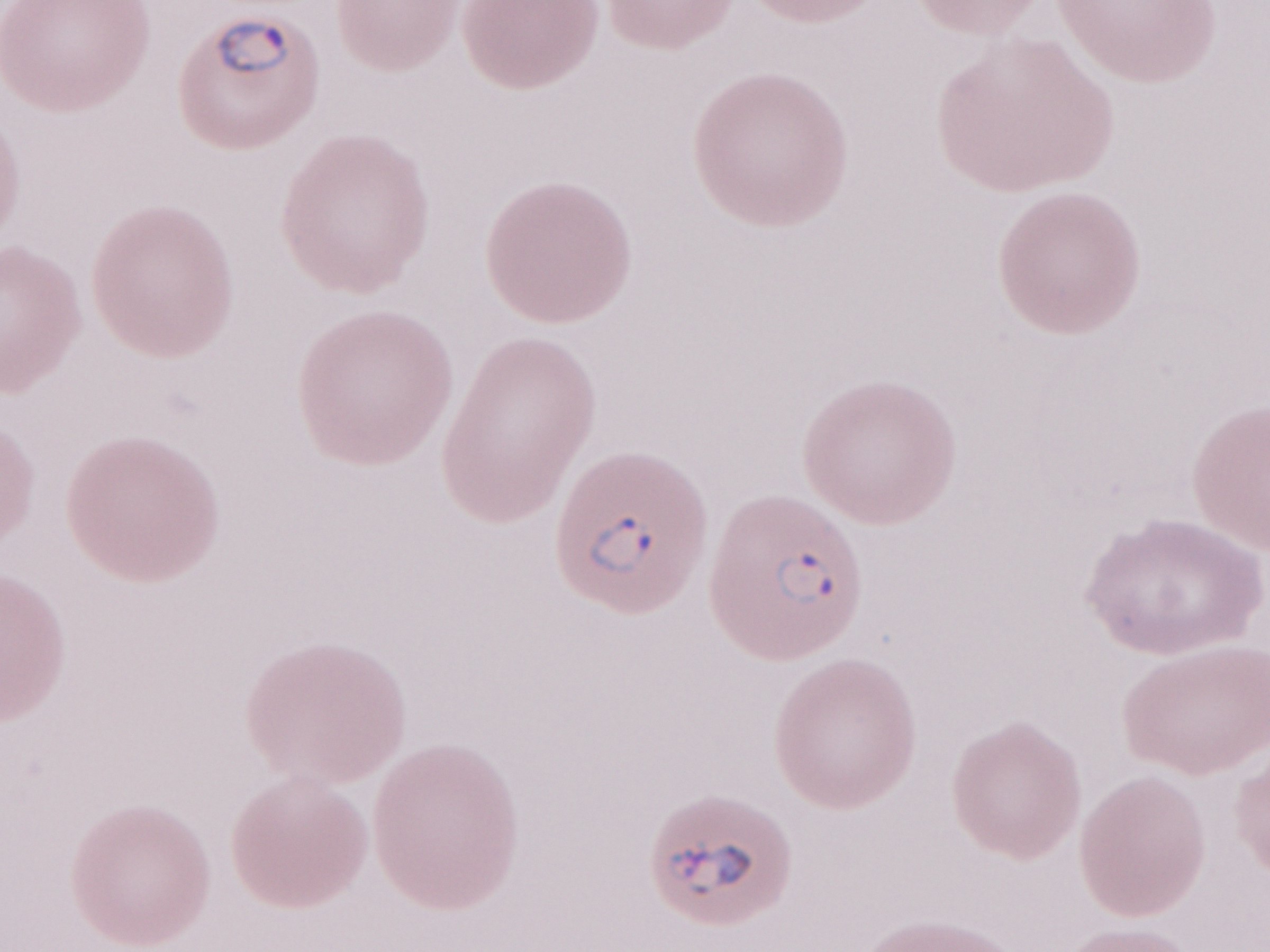
Single field of view. May-Grünwald-Giemsa (MGG) stain. Thin blood film. Image is 1270×952 pixels. Olympus BX43 microscope and DP73 digital camera. Malaria diagnosis (patient-level): positive. Magnification: 1,000x.